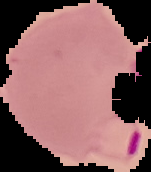 Image is 151×172 pixels. From a thin blood film. Cell region segmented out of the field of view; the surrounding area is masked to black. Malaria status: parasitized.